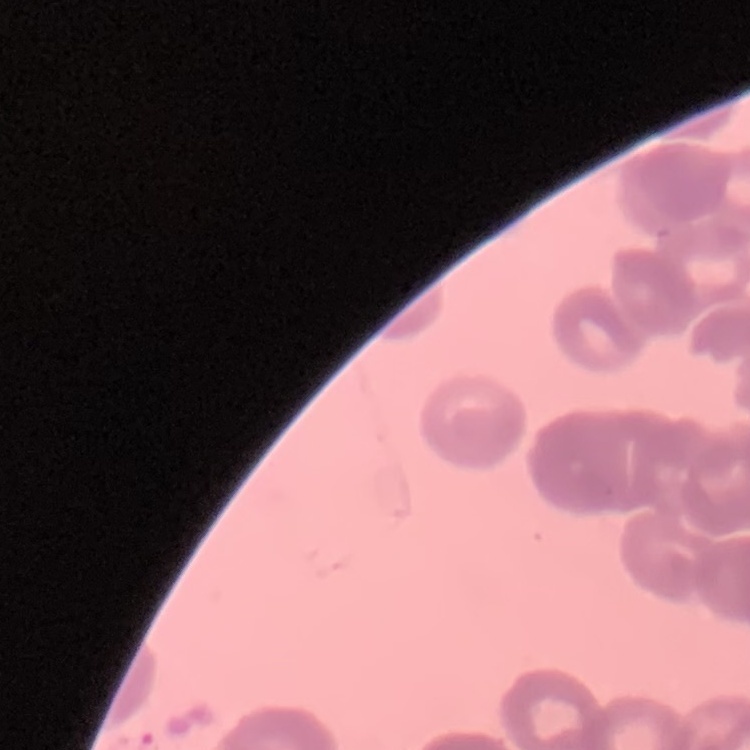 The red blood cells show rouleaux formation. One tile cut from a larger photomicrograph. Stained with either Field's or Giemsa. Thin peripheral smear.